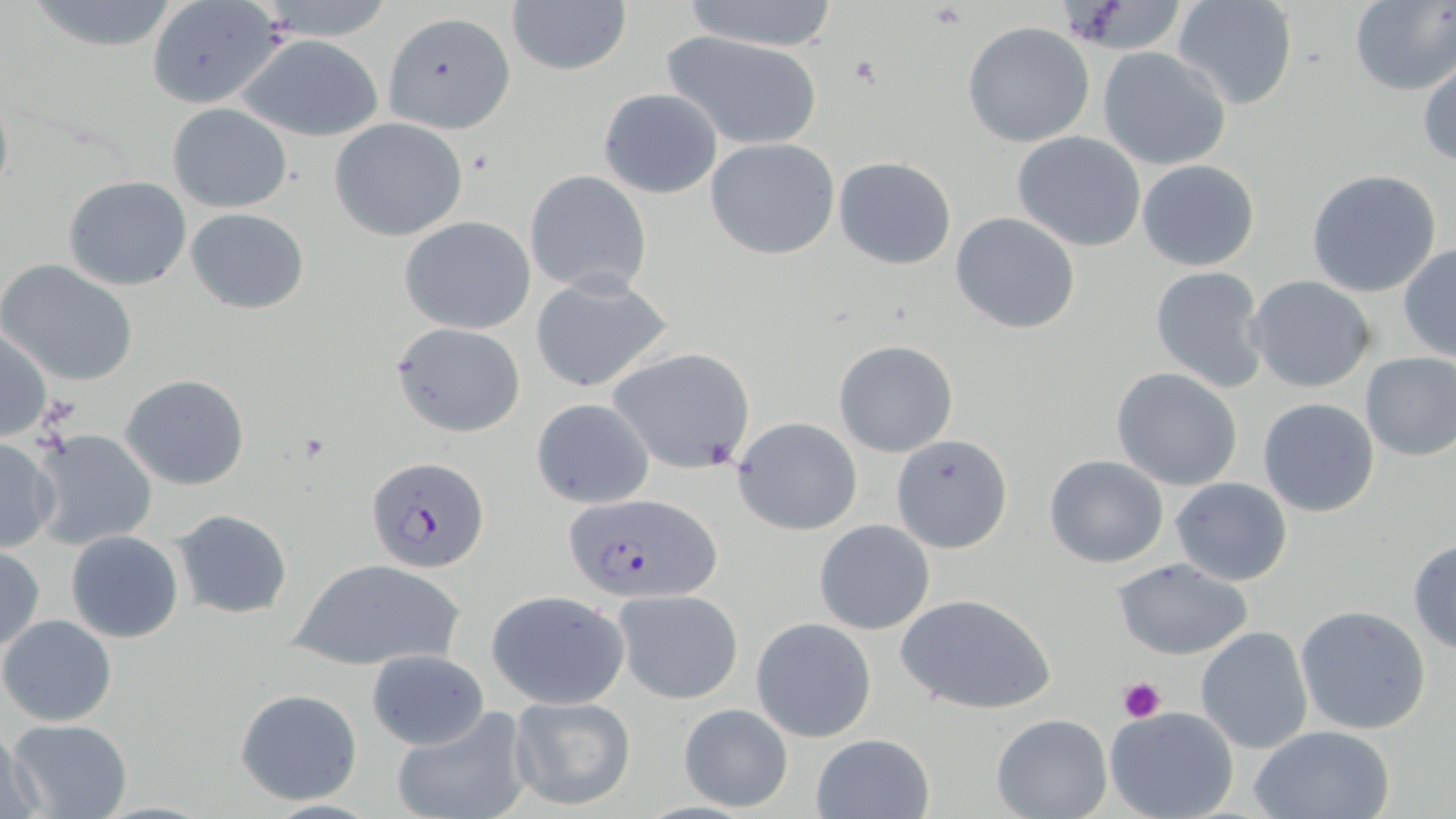
Approximate bounding boxes as (x1,y1)-(x2,y2) corner pairs in pixels. Uninfected red blood cell locations: (677,0)-(842,52), (1170,0)-(1300,111), (1349,0)-(1456,95), (20,1)-(187,50), (145,1)-(287,109), (506,1)-(631,77), (381,12)-(516,134), (962,21)-(1095,148), (661,30)-(824,150), (235,35)-(384,141), (1097,46)-(1235,172), (1418,58)-(1456,166), (598,87)-(723,198), (167,103)-(292,213), (329,117)-(470,242), (1012,130)-(1146,251), (705,138)-(839,259), (833,156)-(956,269), (1136,158)-(1260,271), (1304,169)-(1443,297), (523,170)-(652,296), (62,175)-(191,290), (186,208)-(310,313), (950,213)-(1080,333), (399,215)-(536,334), (1398,245)-(1456,363), (0,260)-(140,386), (1148,265)-(1270,393), (530,273)-(675,395), (1245,274)-(1377,393), (390,322)-(526,437), (0,326)-(51,443), (833,340)-(959,458), (606,345)-(757,475), (1358,352)-(1456,461), (1110,367)-(1244,492), (120,373)-(250,489), (529,397)-(656,509), (1257,397)-(1381,518), (732,417)-(862,536), (28,428)-(159,550), (890,434)-(1012,553), (0,436)-(62,554), (1044,454)-(1168,568), (1170,476)-(1293,586), (171,508)-(294,620), (813,519)-(934,635), (66,531)-(184,642), (1407,538)-(1456,655), (0,546)-(45,653), (1113,558)-(1253,661), (288,559)-(466,671), (612,588)-(744,705), (485,590)-(629,709), (896,593)-(1056,715), (1295,604)-(1432,735), (1,615)-(117,727), (750,618)-(876,742), (1196,625)-(1314,755), (366,650)-(490,749), (233,686)-(365,806), (508,696)-(635,811), (678,703)-(794,814), (388,705)-(536,819), (1104,707)-(1241,819), (989,713)-(1112,819), (4,717)-(132,819), (1247,724)-(1397,819), (2,725)-(47,818), (810,732)-(935,819). Platelet locations: (850,55)-(884,86), (1117,675)-(1166,722). Plasmodium falciparum-infected red blood cell locations: (365,454)-(489,572), (558,494)-(719,604). Slide-level diagnosis: Plasmodium falciparum. 1000x magnification. Single field of view. Light microscopy. May-Grünwald-Giemsa-stained preparation. Thin blood film. Image is 1456×819 pixels.